Identify the preparation type.
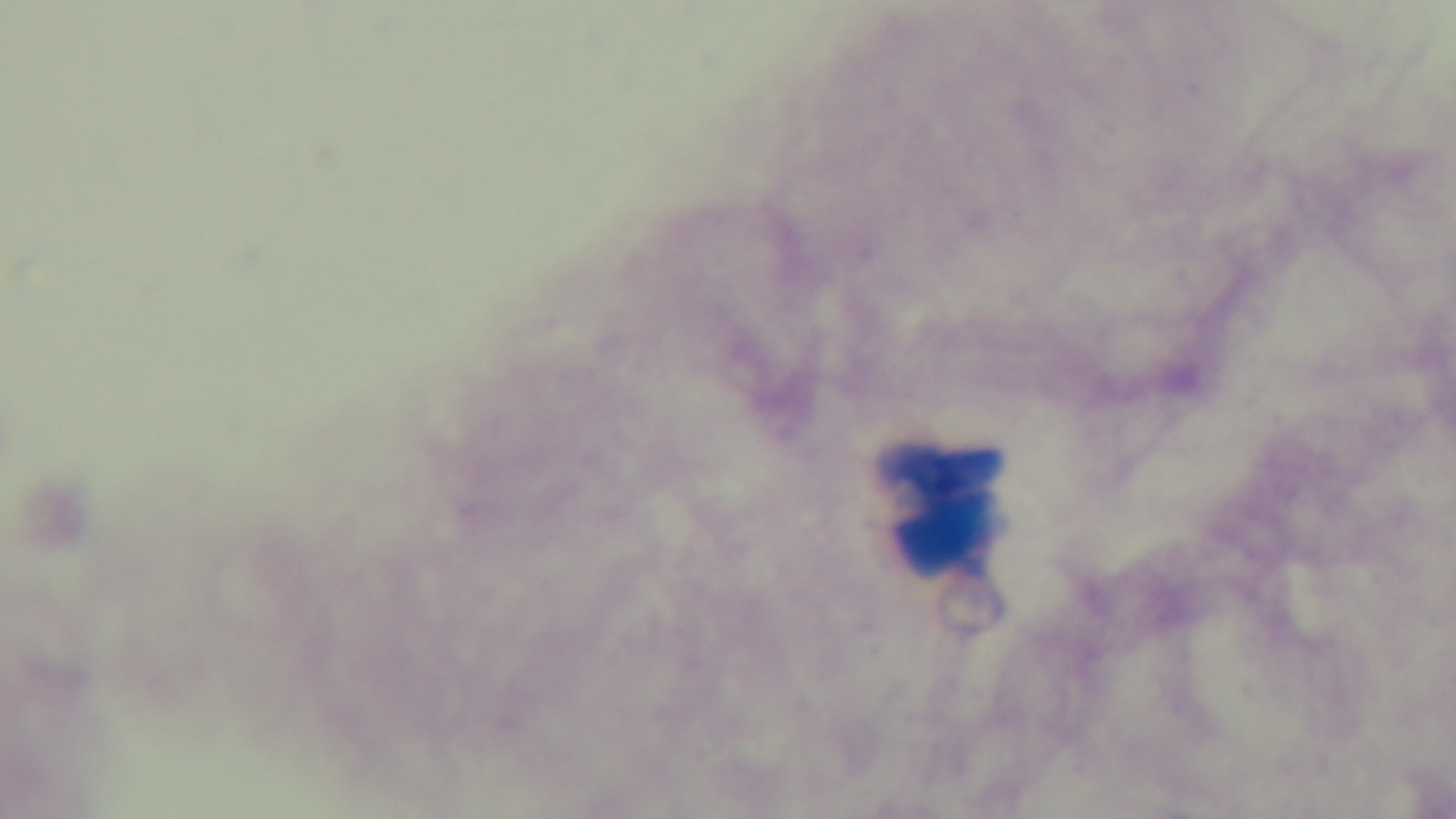
It is a thick blood film.

Giemsa-stained. Single field of view. Oil-immersion objective, 100x. Photomicrograph. Malaria status: uninfected. Captured with a mounted 4K digital camera.